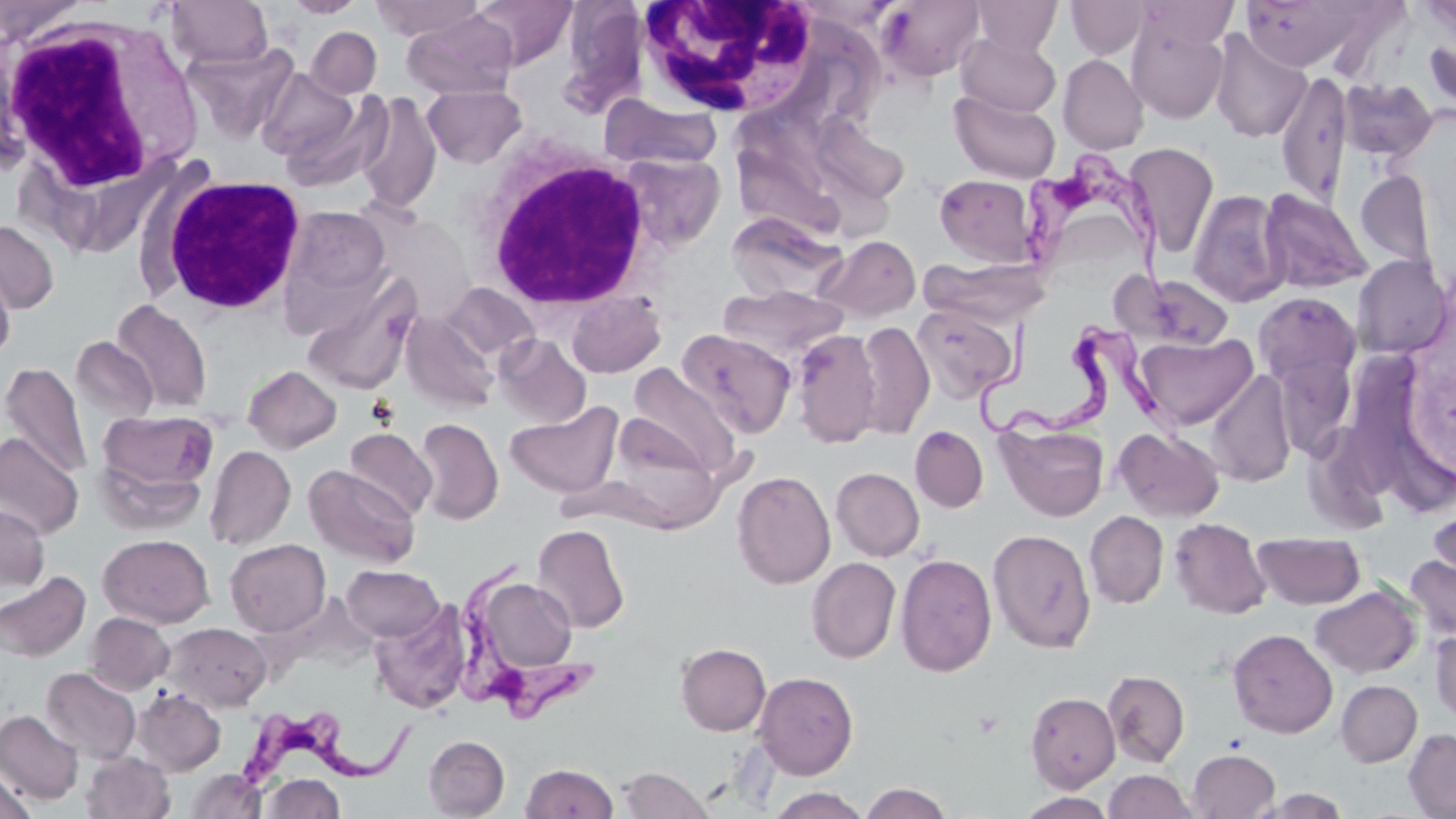
slide-level diagnosis = Trypanosoma brucei
field of view = single
stain = May-Grünwald-Giemsa
preparation = thin blood smear
modality = light microscopy
image size = 1456×819 pixels
magnification = 1000x
Trypanosoma brucei locations = approximate bounding boxes as [x1, y1, x2, y2] in pixels: [1016, 147, 1184, 320], [976, 317, 1176, 451], [456, 560, 599, 726], [239, 713, 432, 800]
uninfected red blood cell locations = approximate bounding boxes as [x1, y1, x2, y2] in pixels: [284, 0, 367, 17], [369, 0, 485, 40], [470, 0, 577, 69], [877, 0, 984, 81], [972, 0, 1062, 54], [1066, 0, 1149, 59], [1135, 0, 1239, 50], [1240, 0, 1369, 72], [0, 1, 86, 43], [166, 1, 274, 69], [403, 10, 517, 98], [1127, 19, 1228, 124], [306, 26, 381, 98], [1209, 29, 1312, 143], [956, 33, 1061, 117], [183, 42, 299, 144], [1058, 54, 1148, 155], [257, 68, 362, 167], [1276, 69, 1353, 206], [1338, 77, 1438, 163], [422, 84, 527, 168], [354, 91, 443, 213], [949, 91, 1061, 183], [599, 93, 723, 171], [811, 116, 910, 204], [1124, 143, 1219, 258], [617, 152, 727, 253], [1356, 170, 1436, 272], [934, 173, 1040, 266], [1258, 188, 1373, 294], [1187, 189, 1290, 307], [280, 205, 391, 312], [727, 214, 847, 303], [0, 221, 59, 315], [816, 235, 920, 322], [1352, 255, 1451, 358], [920, 256, 1051, 325], [0, 259, 16, 362], [302, 271, 420, 396], [1124, 271, 1237, 349], [441, 283, 538, 363], [718, 285, 848, 363], [566, 291, 665, 377], [1253, 291, 1360, 385], [111, 299, 212, 414], [912, 304, 1019, 402], [402, 312, 499, 411], [854, 320, 935, 439], [678, 327, 795, 438], [791, 330, 882, 448], [1134, 332, 1257, 431], [494, 334, 591, 428], [70, 336, 158, 426], [1270, 352, 1358, 458], [1, 362, 92, 480], [243, 364, 341, 453], [628, 364, 742, 479], [1208, 370, 1296, 487], [505, 401, 623, 498], [97, 409, 218, 505], [605, 413, 723, 529], [415, 418, 503, 524], [996, 421, 1109, 522], [910, 425, 988, 512], [1114, 426, 1224, 522], [344, 427, 437, 521], [0, 433, 84, 538], [205, 445, 296, 550], [304, 465, 419, 568], [831, 467, 925, 561], [731, 470, 835, 590], [1427, 500, 1456, 594], [0, 505, 50, 598], [1084, 510, 1168, 608], [1169, 517, 1272, 619], [532, 524, 630, 633], [988, 528, 1096, 653], [1253, 532, 1365, 609], [98, 534, 215, 628], [225, 538, 331, 636], [895, 553, 996, 677], [1404, 553, 1456, 644], [806, 557, 901, 662], [341, 565, 444, 642], [0, 571, 90, 663], [472, 575, 579, 676], [1310, 585, 1421, 678], [370, 602, 471, 714], [85, 612, 174, 695], [164, 622, 271, 711], [1228, 628, 1337, 738], [1430, 629, 1456, 723], [676, 642, 770, 735], [41, 667, 141, 764], [1103, 669, 1190, 767], [754, 671, 859, 779], [1336, 679, 1422, 767], [132, 688, 226, 775], [1025, 691, 1119, 791], [0, 710, 84, 805], [1404, 728, 1456, 818], [423, 735, 510, 818], [1187, 749, 1280, 818], [81, 751, 174, 819], [520, 763, 620, 818], [618, 766, 714, 818], [184, 768, 266, 818], [0, 770, 36, 817], [1104, 770, 1197, 819], [261, 773, 345, 818], [859, 782, 954, 819], [765, 787, 871, 819], [1254, 789, 1352, 818], [1017, 792, 1118, 818]
white blood cell locations = approximate bounding boxes as [x1, y1, x2, y2] in pixels: [633, 4, 820, 120], [0, 9, 205, 226], [422, 82, 533, 169], [470, 135, 658, 312], [154, 174, 307, 316]